Assess this cell for malaria.
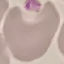
It is uninfected.

Summary:
  - Image type: automatically extracted cell patch, resized to 64 × 64 pixels
  - Preparation: thin blood film
  - Capture: smartphone camera at the microscope eyepiece
  - Stain: Giemsa